Locate every blood parasite and identify its species.
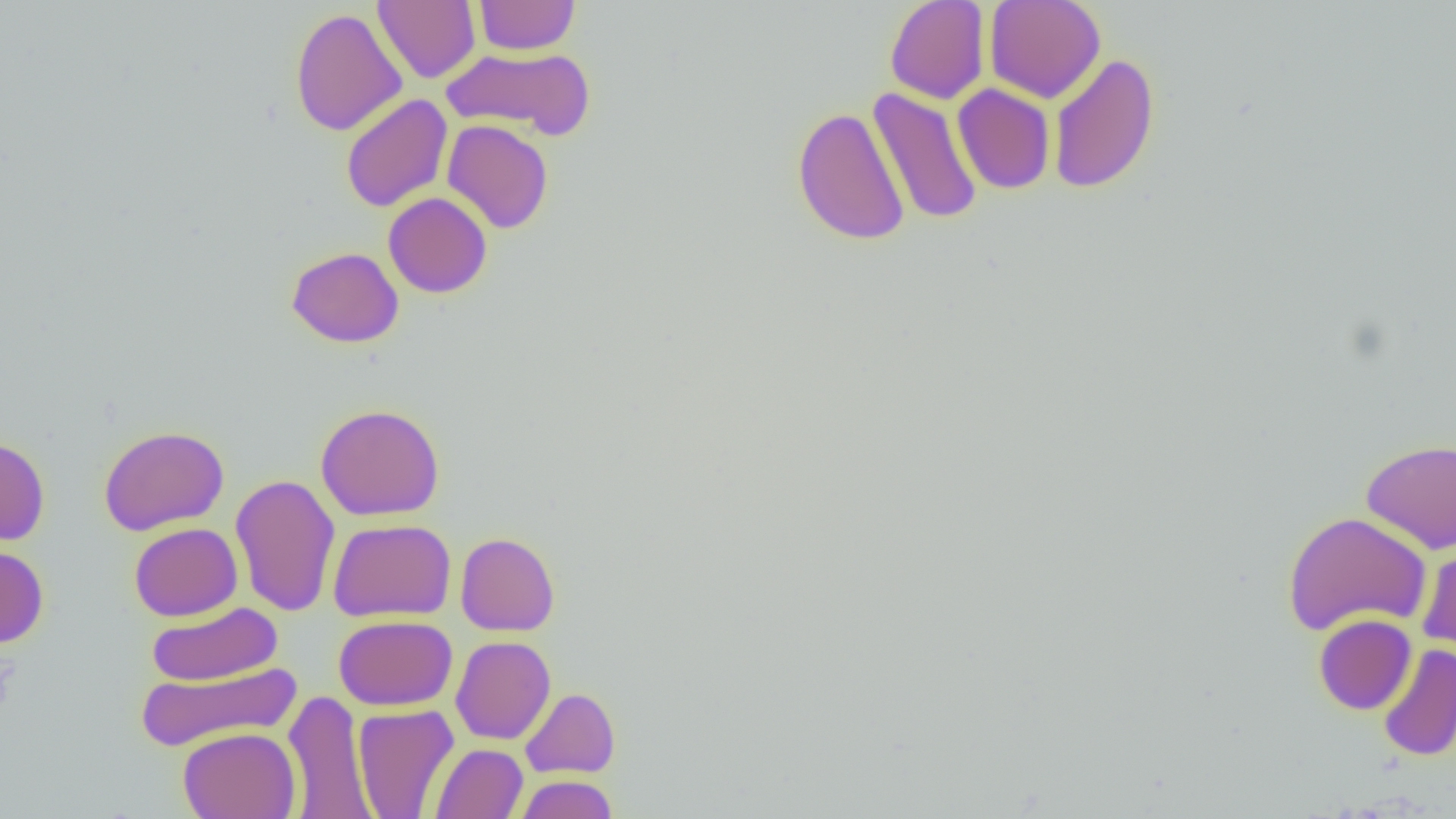
No blood parasites seen.

Summary:
  - Coordinate format: approximate bounding boxes as (x1, y1, x2, y2) in pixels
  - Uninfected red blood cell locations: (373, 0, 481, 83), (474, 0, 579, 55), (884, 0, 991, 104), (984, 0, 1106, 103), (290, 7, 407, 137), (442, 46, 595, 140), (1048, 53, 1161, 194), (952, 83, 1055, 194), (868, 87, 983, 226), (340, 94, 453, 212), (792, 106, 910, 246), (442, 119, 554, 234), (383, 192, 492, 298), (287, 246, 404, 348), (315, 403, 445, 520), (98, 425, 230, 536), (0, 436, 50, 546), (1361, 439, 1456, 554), (230, 474, 340, 616), (1283, 511, 1432, 637), (328, 518, 456, 621), (129, 522, 242, 621), (456, 532, 559, 636), (1417, 540, 1456, 665), (0, 544, 49, 648), (146, 601, 283, 686), (1313, 614, 1417, 715), (333, 615, 458, 711), (451, 635, 556, 745), (1378, 644, 1456, 763), (135, 661, 302, 752), (520, 688, 621, 779), (283, 690, 375, 819), (352, 704, 460, 818), (178, 726, 301, 819), (429, 743, 527, 819), (514, 775, 618, 818)
  - Slide-level diagnosis: negative for blood parasites
  - Field of view: one of a larger specimen
  - Preparation: thin blood film
  - Magnification: 1000x
  - Image size: 1456×819 pixels
  - Modality: light microscopy